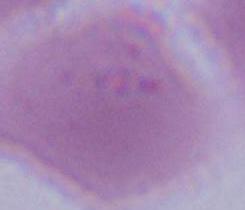

Captured at 1000x magnification. An erythrocyte is seen. Micrograph.